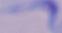 Micrograph. A trypanosome is shown. Captured at 1000x magnification.